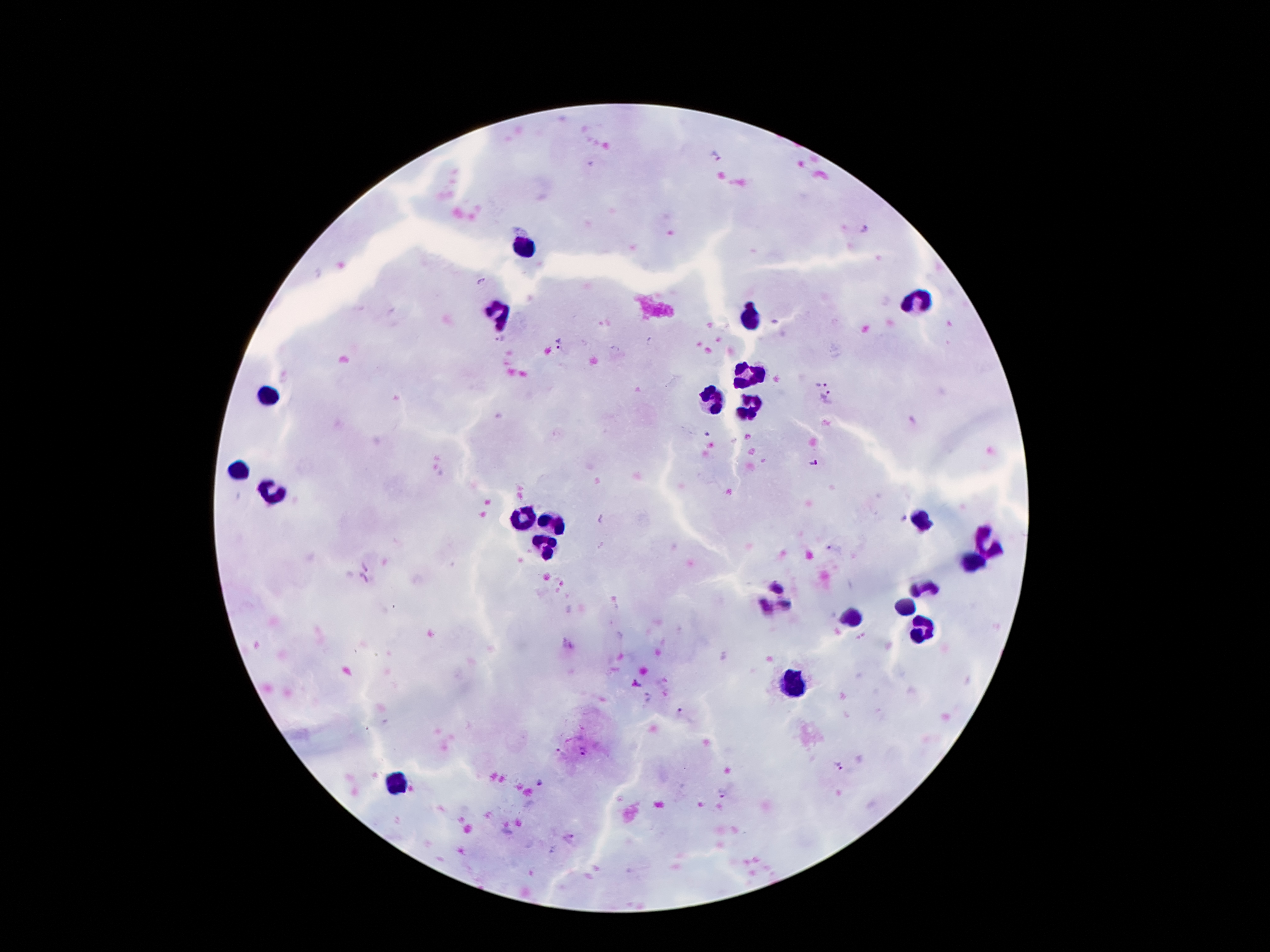
coordinate format = approximate object centers, in pixels from the top-left corner
leukocyte locations = (x=525, y=246), (x=918, y=303), (x=502, y=315), (x=752, y=322), (x=752, y=377), (x=268, y=395), (x=713, y=399), (x=748, y=406), (x=238, y=469), (x=275, y=492), (x=527, y=518), (x=922, y=520), (x=555, y=522), (x=988, y=543), (x=545, y=545), (x=978, y=559), (x=926, y=590), (x=906, y=610), (x=853, y=621), (x=924, y=629), (x=795, y=682), (x=400, y=785)
malaria parasite locations = (x=716, y=159), (x=864, y=231), (x=481, y=282), (x=498, y=340), (x=557, y=342), (x=821, y=385), (x=828, y=396), (x=812, y=463), (x=368, y=565), (x=363, y=580), (x=582, y=751), (x=561, y=753), (x=841, y=766), (x=541, y=783), (x=723, y=792), (x=569, y=840)
stain = Giemsa
preparation = thick blood smear
capture = smartphone camera through the microscope eyepiece
field of view = single
magnification = 100x
image size = 1270×952 pixels
patient malaria status = positive for Plasmodium falciparum